Point out each leukocyte.
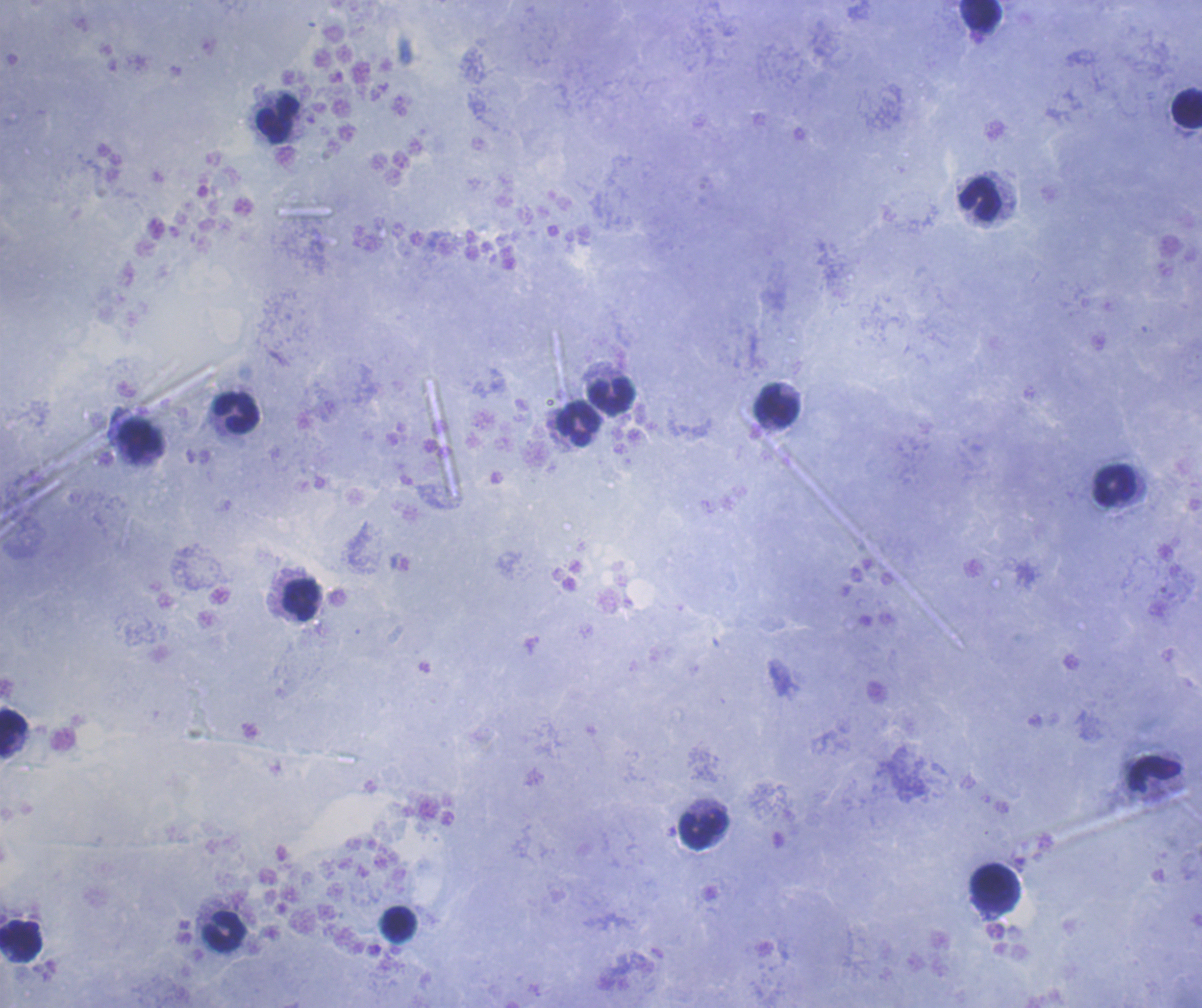

Approximate object centers, in pixels from the top-left corner.
Leukocytes: (x=979, y=15), (x=1187, y=108), (x=278, y=119), (x=980, y=199), (x=610, y=396), (x=777, y=405), (x=236, y=412), (x=578, y=423), (x=141, y=442), (x=1114, y=485), (x=301, y=600), (x=12, y=732), (x=1154, y=773), (x=702, y=830), (x=996, y=888), (x=398, y=924), (x=224, y=931), (x=20, y=942).

result = negative for Plasmodium parasites
preparation = thick blood smear
context = previously used in a real diagnosis
background quality = good
image size = 1202×1008 pixels
stain = Romanowsky
coloration quality = good
magnification = 100x
field of view = single